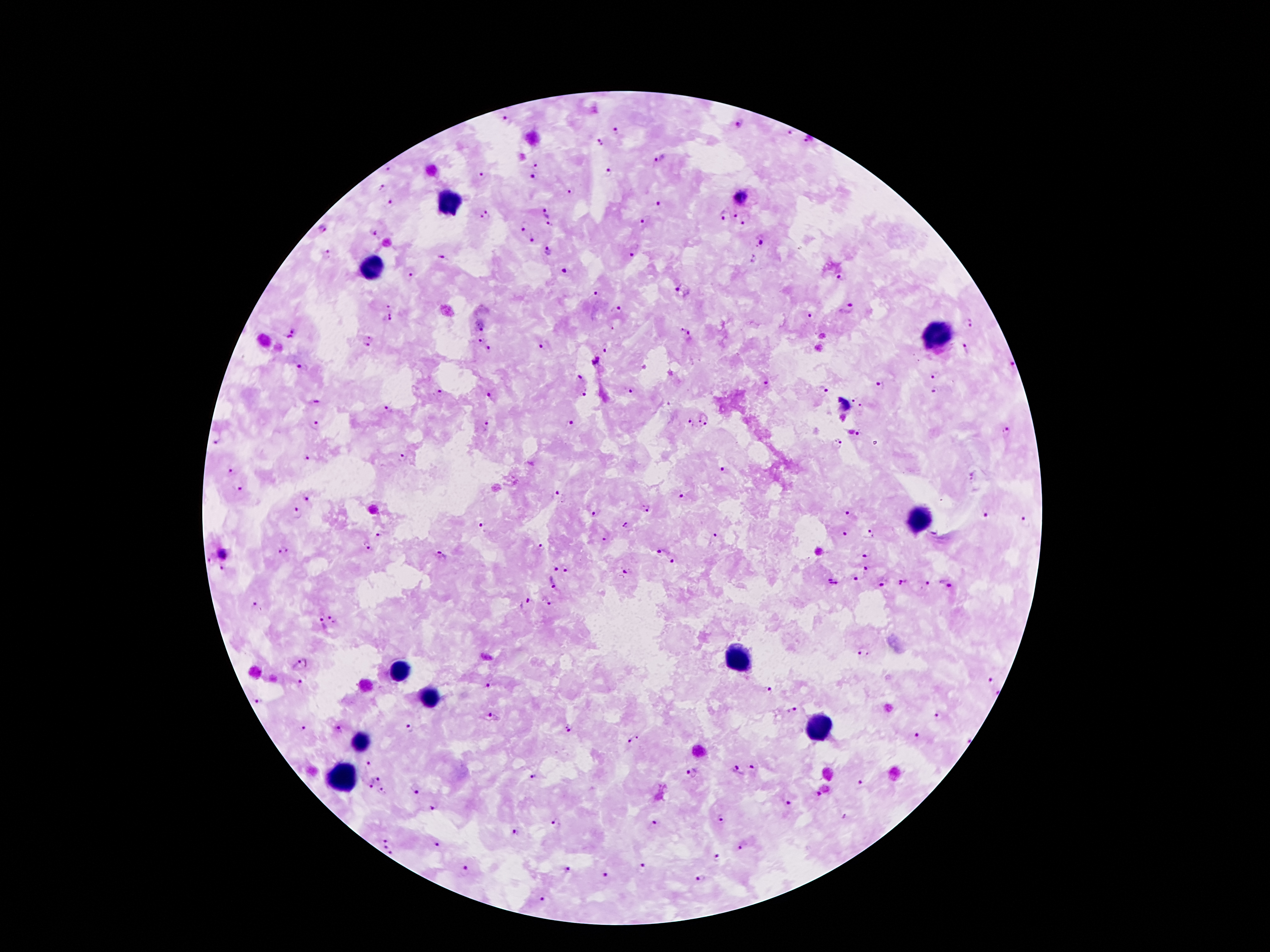

{
  "plasmodium_parasite_locations": "approximate object centers, in pixels from the top-left corner: (x=505, y=119), (x=739, y=124), (x=616, y=130), (x=792, y=131), (x=600, y=141), (x=809, y=141), (x=661, y=159), (x=537, y=165), (x=389, y=169), (x=610, y=174), (x=483, y=175), (x=534, y=178), (x=380, y=187), (x=571, y=192), (x=741, y=197), (x=390, y=203), (x=661, y=204), (x=543, y=210), (x=735, y=212), (x=723, y=213), (x=486, y=216), (x=747, y=218), (x=643, y=222), (x=550, y=224), (x=521, y=225), (x=322, y=229), (x=374, y=232), (x=532, y=238), (x=760, y=243), (x=547, y=252), (x=632, y=252), (x=327, y=254), (x=441, y=258), (x=563, y=270), (x=410, y=276), (x=843, y=278), (x=678, y=289), (x=598, y=293), (x=390, y=306), (x=618, y=308), (x=848, y=308), (x=811, y=315), (x=387, y=319), (x=970, y=322), (x=480, y=325), (x=295, y=330), (x=685, y=334), (x=290, y=339), (x=369, y=339), (x=480, y=341), (x=544, y=344), (x=488, y=349), (x=608, y=349), (x=964, y=349), (x=595, y=360), (x=1012, y=364), (x=299, y=367), (x=934, y=374), (x=579, y=377), (x=767, y=384), (x=879, y=385), (x=824, y=390), (x=631, y=391), (x=934, y=391), (x=440, y=393), (x=489, y=394), (x=584, y=394), (x=854, y=398), (x=317, y=399), (x=845, y=406), (x=863, y=406), (x=388, y=407), (x=705, y=418), (x=489, y=422), (x=689, y=422), (x=570, y=424), (x=315, y=425), (x=1007, y=431), (x=859, y=432), (x=214, y=439), (x=837, y=444), (x=403, y=457), (x=308, y=458), (x=723, y=469), (x=232, y=471), (x=239, y=485), (x=559, y=494), (x=681, y=495), (x=308, y=499), (x=646, y=509), (x=848, y=511), (x=296, y=513), (x=595, y=513), (x=984, y=514), (x=1024, y=521), (x=627, y=524), (x=480, y=526), (x=715, y=534), (x=843, y=534), (x=870, y=534), (x=378, y=535), (x=604, y=541), (x=366, y=545), (x=541, y=547), (x=283, y=550), (x=659, y=552), (x=222, y=553), (x=866, y=553), (x=440, y=556), (x=210, y=560), (x=671, y=560), (x=221, y=567), (x=555, y=568), (x=567, y=568), (x=865, y=569), (x=625, y=571), (x=857, y=578), (x=903, y=581), (x=834, y=582), (x=946, y=582), (x=554, y=583), (x=926, y=584), (x=882, y=585), (x=546, y=601), (x=255, y=604), (x=526, y=604), (x=334, y=616), (x=320, y=625), (x=864, y=654), (x=303, y=665), (x=989, y=679), (x=302, y=682), (x=489, y=684), (x=768, y=692), (x=997, y=693), (x=255, y=701), (x=795, y=709), (x=938, y=715), (x=495, y=716), (x=304, y=727), (x=338, y=727), (x=409, y=727), (x=569, y=728), (x=915, y=737), (x=633, y=739), (x=966, y=740), (x=370, y=763), (x=752, y=767), (x=737, y=770), (x=694, y=773), (x=533, y=777), (x=378, y=779), (x=860, y=783), (x=370, y=787), (x=381, y=790), (x=417, y=790), (x=819, y=793), (x=787, y=804), (x=432, y=807), (x=720, y=820), (x=557, y=823), (x=655, y=824), (x=515, y=832), (x=385, y=839), (x=433, y=845), (x=385, y=847), (x=741, y=848), (x=390, y=851), (x=718, y=858), (x=464, y=867), (x=570, y=868), (x=641, y=869), (x=602, y=875), (x=699, y=878), (x=543, y=897)",
  "patient_malaria_status": "positive for Plasmodium falciparum",
  "image_size": "1270×952 pixels",
  "preparation": "thick peripheral-blood smear",
  "stain": "Giemsa",
  "leukocyte_locations": "approximate object centers, in pixels from the top-left corner: (x=450, y=198), (x=372, y=270), (x=940, y=335), (x=923, y=520), (x=739, y=658), (x=400, y=669), (x=428, y=698), (x=818, y=723), (x=359, y=744), (x=342, y=779)",
  "capture": "smartphone camera through the microscope eyepiece",
  "field_of_view": "single",
  "magnification": "100x"
}